Assess this cell for malaria.
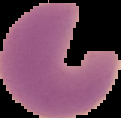
It is parasitized.

{
  "image_size": "121×118 pixels",
  "preparation": "thin blood smear",
  "image_type": "segmented cell region with the area outside set to black"
}